Classify this cell by malaria status.
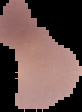

Uninfected.

Image is 82×112 pixels. The area outside the segmented cell region is set to black. From a thin blood smear.